Describe the morphology of the red blood cells.
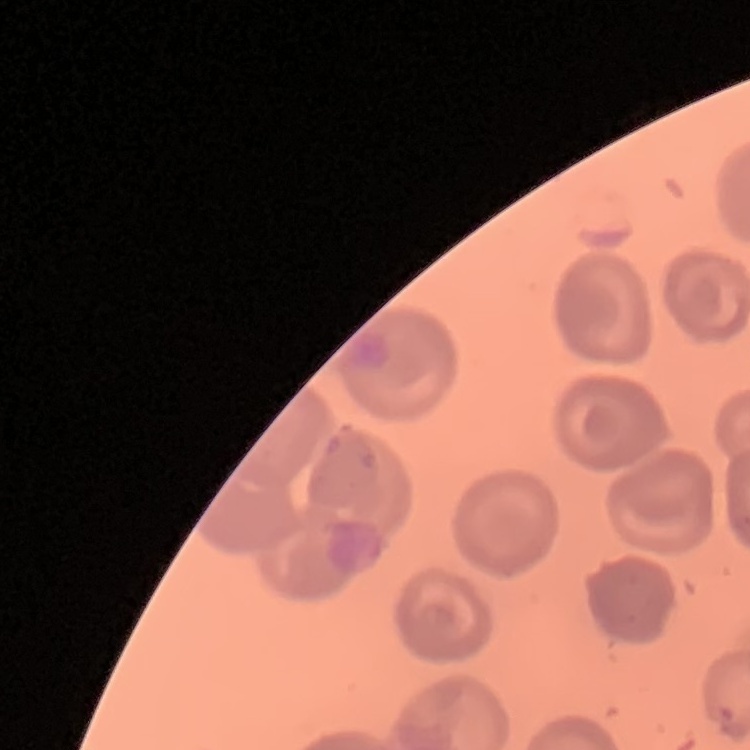
They show no rouleaux formation.

image_type: one tile cut from a larger photomicrograph
preparation: thin blood film
stain: Field's or Giemsa